Assess this cell for malaria.
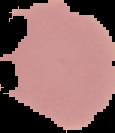
It is uninfected.

image_type: segmented cell region with the area outside set to black
image_size: 115×133 pixels
preparation: thin blood film